Assess this cell for malaria.
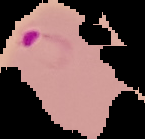
It is parasitized.

Cell region segmented out of the field of view; the surrounding area is masked to black. From a thin blood film. Image is 145×139 pixels.